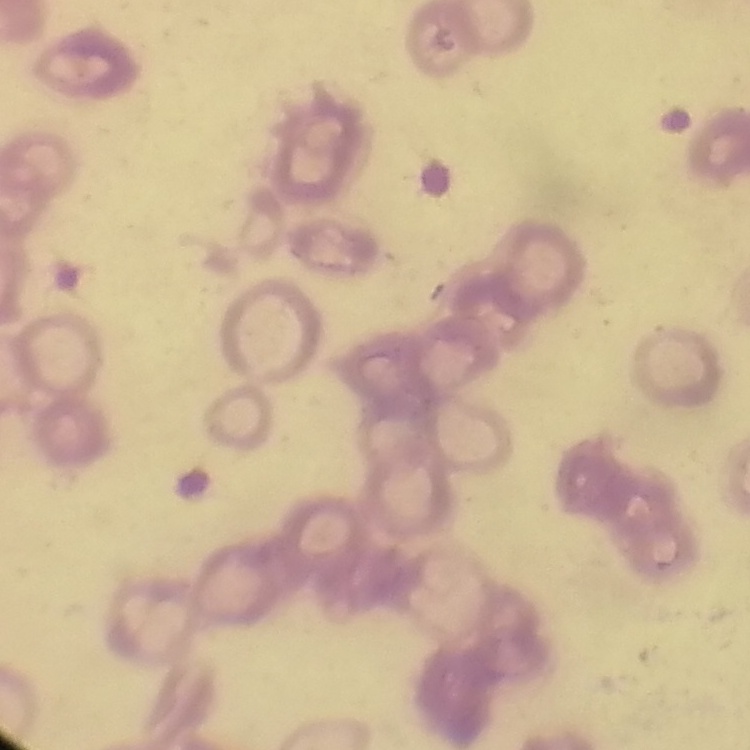

red_blood_cell_morphology: rouleaux formation
stain: Field's or Giemsa
image_type: one tile cut from a larger photomicrograph
preparation: thin blood smear